Report the malaria status of this cell.
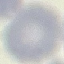

Uninfected.

Giemsa stain. Cell patch, automatically extracted from a larger field of view and resized to 64 × 64 pixels. Thin blood film. Photographed with a smartphone camera at the microscope eyepiece.